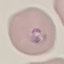
Summary:
  - Result: malaria parasites detected
  - Preparation: thin smear
  - Capture: smartphone camera at the microscope eyepiece
  - Image type: automatically extracted cell patch, resized to 64 × 64 pixels
  - Stain: Giemsa